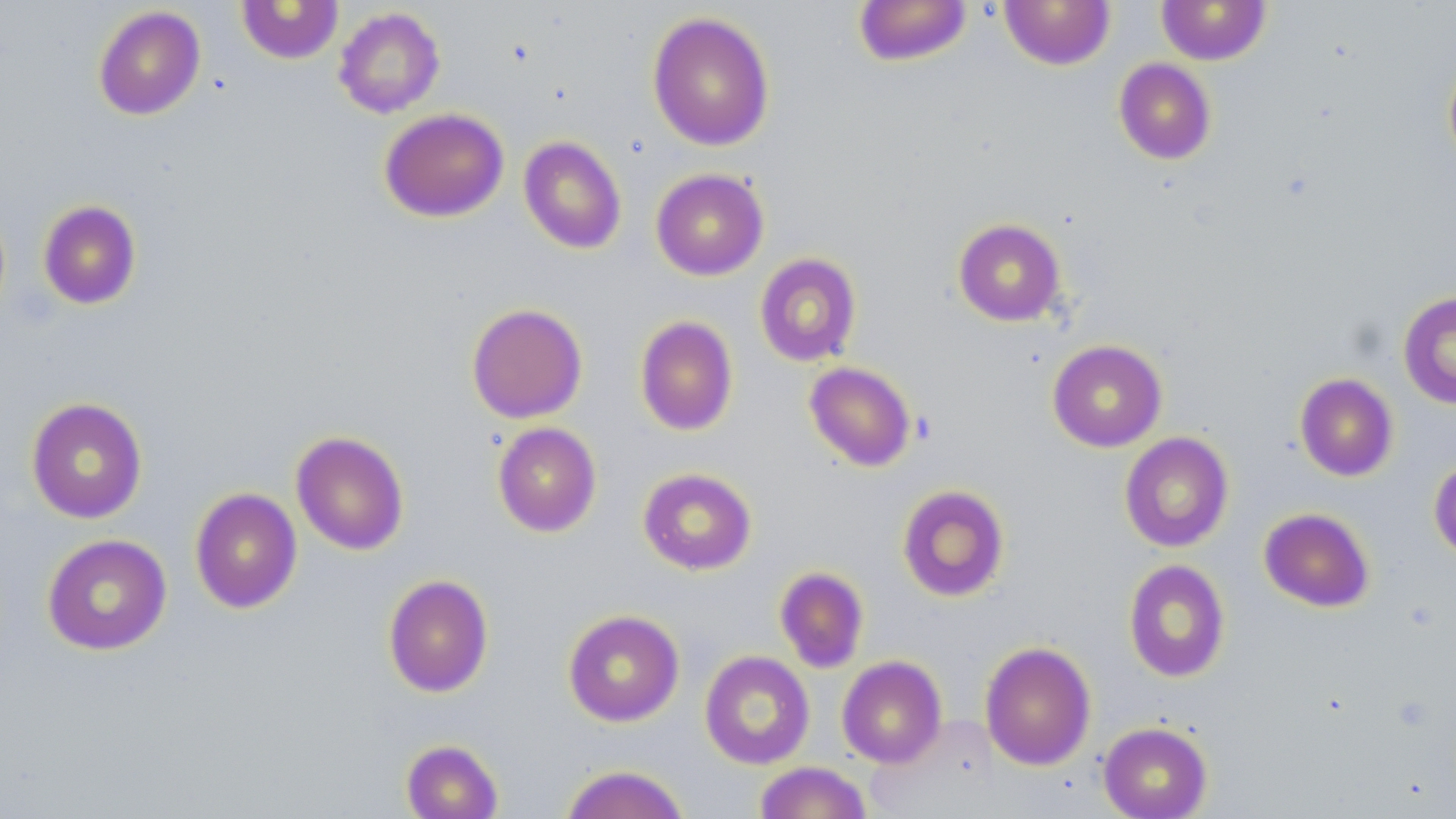

Approximate bounding boxes as [x1, y1, x2, y2] in pixels. Uninfected red blood cell locations: [853, 0, 973, 67], [998, 0, 1116, 71], [236, 1, 343, 64], [1157, 1, 1271, 65], [93, 5, 206, 120], [333, 6, 446, 118], [646, 11, 775, 152], [1442, 52, 1456, 173], [1113, 58, 1216, 165], [379, 108, 509, 222], [518, 136, 627, 255], [651, 168, 769, 281], [37, 200, 142, 309], [953, 218, 1067, 326], [754, 252, 862, 367], [1398, 290, 1456, 409], [466, 303, 588, 424], [634, 315, 738, 436], [1047, 339, 1167, 452], [804, 361, 916, 472], [1294, 373, 1398, 481], [25, 396, 148, 524], [492, 422, 601, 537], [291, 431, 409, 555], [1119, 432, 1234, 552], [1429, 457, 1456, 563], [637, 467, 757, 575], [896, 484, 1009, 602], [189, 487, 303, 614], [1259, 507, 1374, 612], [41, 533, 172, 656], [1123, 559, 1230, 682], [774, 566, 869, 673], [383, 574, 494, 698], [562, 609, 685, 727], [980, 641, 1096, 770], [699, 650, 815, 769], [836, 656, 947, 768], [1098, 721, 1213, 819], [400, 739, 503, 819], [753, 761, 871, 819], [559, 764, 690, 819]. Slide-level diagnosis: negative for blood parasites. Thin blood film. Captured at 1000x magnification. One field of a larger specimen. May-Grünwald-Giemsa stain. Light microscopy. Image is 1456×819 pixels.